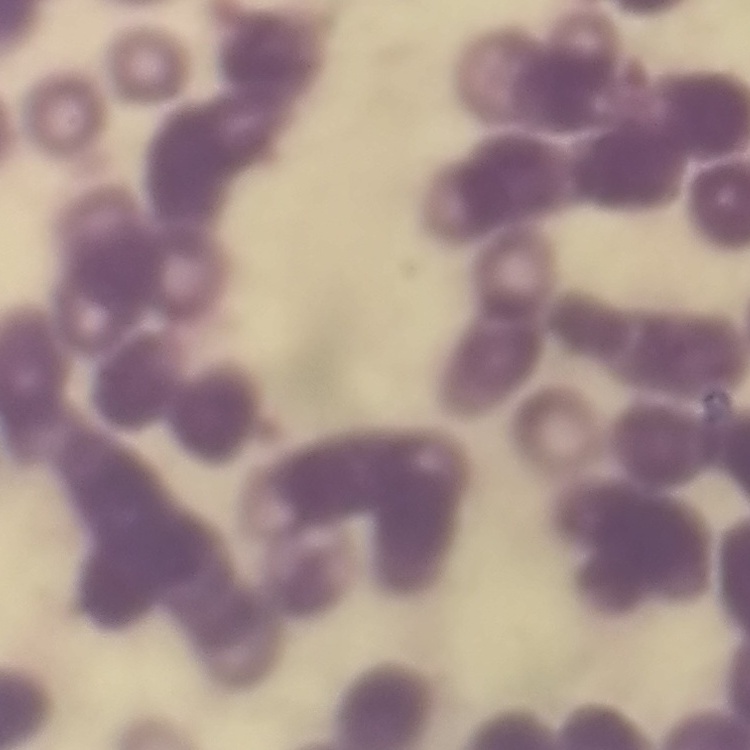

Summary:
  - Erythrocyte morphology: rouleaux formation
  - Image type: one tile cut from a larger photomicrograph
  - Preparation: thin peripheral smear
  - Stain: Field's or Giemsa